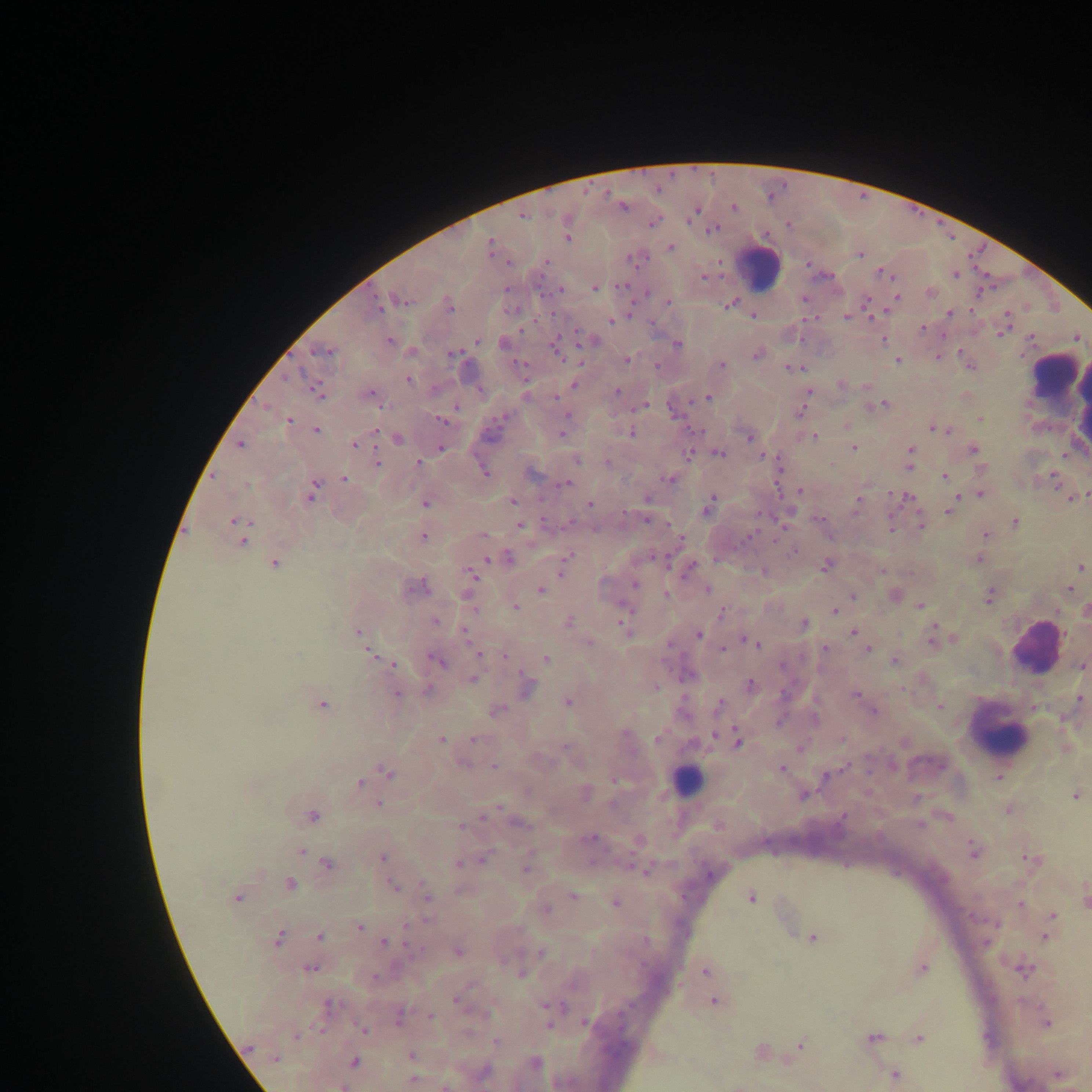

Approximate centers as [x, y] in pixels.
Summary:
  - Plasmodium parasite locations: [623, 206], [734, 207], [695, 210], [522, 215], [653, 222], [713, 229], [568, 235], [490, 247], [670, 247], [859, 253], [545, 262], [808, 264], [883, 273], [956, 274], [703, 276], [594, 288], [560, 289], [930, 292], [804, 298], [896, 298], [400, 300], [866, 301], [668, 302], [730, 303], [376, 304], [449, 305], [950, 313], [752, 315], [847, 316], [610, 321], [1004, 326], [923, 328], [1075, 336], [389, 340], [477, 340], [883, 340], [592, 341], [504, 343], [677, 344], [555, 346], [323, 351], [958, 351], [452, 353], [757, 354], [938, 357], [627, 359], [897, 360], [721, 365], [970, 365], [792, 367], [407, 379], [574, 384], [841, 384], [316, 389], [616, 391], [808, 391], [370, 394], [556, 397], [707, 397], [881, 404], [641, 406], [672, 411], [800, 411], [979, 418], [441, 420], [288, 421], [848, 426], [934, 427], [315, 430], [562, 433], [631, 433], [813, 436], [397, 438], [748, 438], [354, 443], [241, 444], [853, 446], [441, 447], [973, 449], [911, 450], [718, 453], [688, 454], [761, 454], [576, 459], [376, 463], [418, 463], [910, 465], [778, 466], [981, 468], [484, 472], [532, 472], [944, 476], [1054, 477], [668, 478], [344, 479], [567, 483], [800, 491], [311, 493], [981, 494], [958, 495], [907, 497], [1072, 497], [647, 499], [513, 500], [858, 501], [425, 502], [589, 503], [708, 505], [949, 509], [646, 520], [236, 521], [1015, 522], [519, 524], [921, 525], [890, 527], [749, 535], [984, 535], [423, 536], [679, 537], [243, 540], [795, 550], [507, 558], [566, 558], [978, 558], [488, 559], [274, 563], [826, 565], [1080, 566], [688, 568], [562, 570], [764, 571], [471, 574], [634, 584], [415, 586], [1068, 588], [540, 589], [707, 590], [853, 596], [894, 596], [989, 596], [920, 605], [516, 606], [834, 610], [1085, 611], [722, 612], [435, 621], [568, 622], [625, 623], [803, 624], [358, 631], [464, 631], [853, 631], [698, 634], [933, 638], [753, 641], [589, 642], [825, 648], [723, 649], [868, 649], [370, 653], [478, 654], [504, 657], [546, 659], [438, 660], [895, 661], [392, 664], [1082, 665], [472, 679], [750, 684], [526, 687], [428, 689], [396, 694], [855, 695], [1080, 699], [568, 701], [718, 703], [321, 705], [939, 706], [496, 710], [873, 711], [658, 738], [441, 739], [473, 739], [737, 740], [801, 747], [566, 748], [494, 767], [780, 768], [388, 773], [1000, 775], [616, 780], [359, 782], [585, 793], [803, 794], [1074, 794], [378, 803], [1008, 810], [488, 813], [311, 816], [519, 822], [460, 826], [590, 838], [638, 839], [973, 849], [301, 851], [382, 858], [482, 860], [1031, 860], [458, 863], [327, 864], [526, 868], [645, 870], [289, 885], [393, 886], [426, 895], [572, 895], [751, 897], [237, 898], [1084, 898], [615, 902], [1020, 904], [546, 909], [1053, 916], [1050, 924], [359, 927], [1047, 933], [319, 935], [813, 937], [277, 938], [384, 942], [458, 951], [541, 953], [310, 967], [922, 967], [1023, 969], [705, 970], [521, 973], [456, 999], [714, 1000], [328, 1005], [398, 1016], [430, 1016], [584, 1022], [1045, 1022], [364, 1030], [873, 1037], [919, 1038], [496, 1043], [801, 1044], [247, 1048], [760, 1051], [412, 1056], [275, 1058], [354, 1062], [534, 1063], [483, 1072], [1059, 1074], [894, 1075], [413, 1080], [445, 1085], [737, 1085], [343, 1086]
  - Leukocyte locations: [758, 267], [1057, 391], [1037, 647], [998, 731], [686, 781]
  - Field of view: single
  - Capture: mobile-phone photograph through a microscope
  - Preparation: thick blood smear
  - Country: Ghana
  - Image size: 1092×1092 pixels